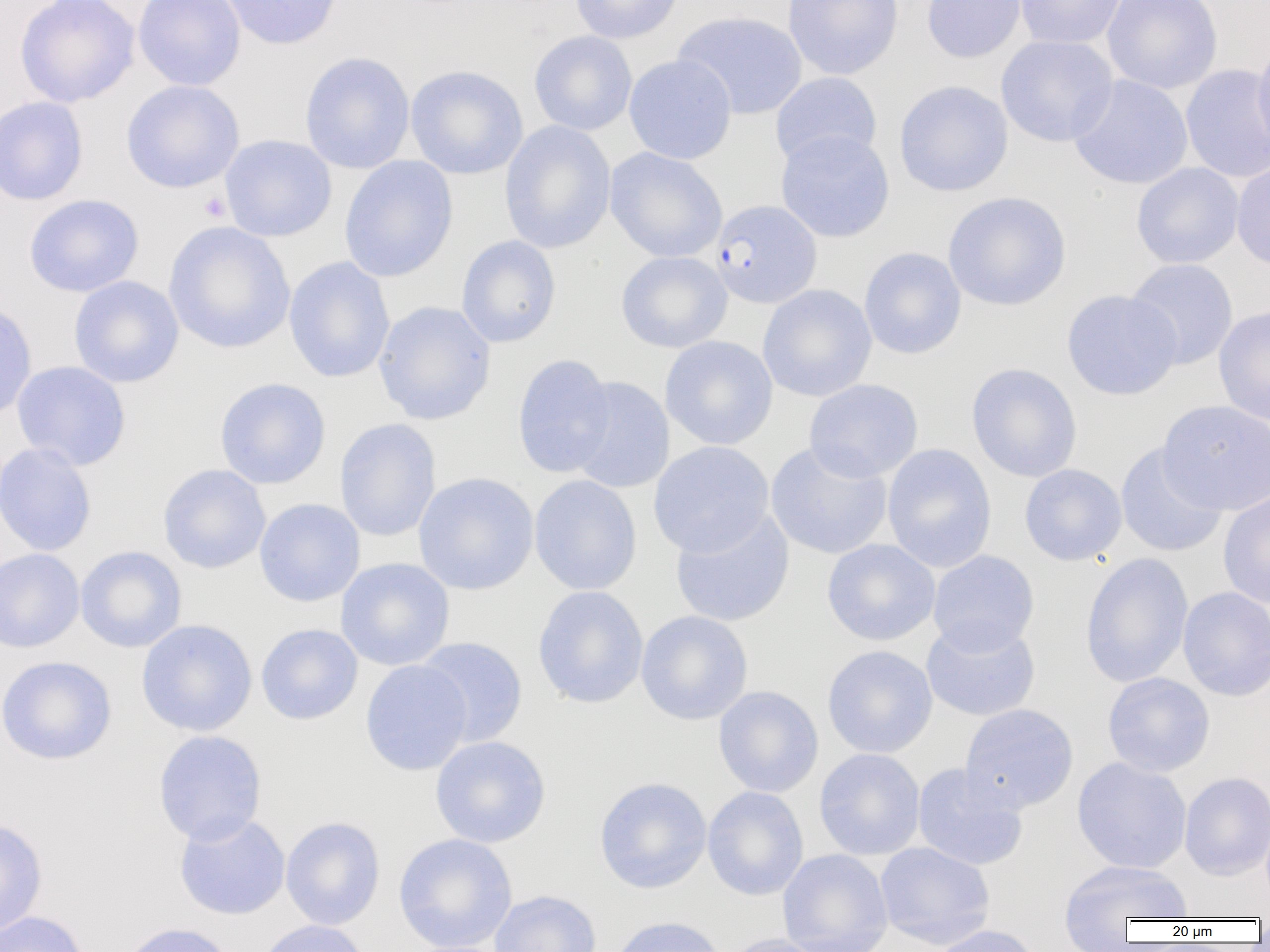 Approximate bounding boxes as [x1, y1, x2, y2] in pixels. Plasmodium falciparum-infected red blood cell locations: [710, 199, 822, 308]. Platelet locations: [199, 192, 232, 222]. Uninfected red blood cell locations: [15, 0, 140, 107], [133, 0, 245, 91], [220, 0, 344, 50], [569, 0, 683, 44], [783, 0, 904, 80], [921, 0, 1028, 63], [1014, 0, 1127, 49], [1102, 0, 1223, 94], [672, 10, 807, 120], [529, 31, 638, 136], [996, 34, 1118, 147], [1252, 36, 1270, 157], [299, 51, 415, 174], [624, 54, 737, 165], [1180, 63, 1270, 183], [406, 65, 528, 179], [770, 72, 882, 168], [1069, 75, 1193, 190], [121, 80, 244, 193], [894, 80, 1013, 197], [0, 95, 89, 206], [499, 120, 617, 254], [775, 129, 895, 243], [219, 134, 337, 242], [604, 147, 727, 262], [339, 156, 459, 283], [1232, 161, 1270, 272], [1131, 163, 1244, 268], [943, 191, 1072, 311], [23, 194, 144, 297], [164, 221, 295, 355], [456, 235, 561, 348], [859, 246, 967, 359], [616, 251, 733, 353], [283, 256, 395, 383], [1125, 258, 1238, 370], [68, 275, 184, 388], [757, 284, 877, 402], [1062, 289, 1182, 400], [0, 299, 37, 422], [373, 301, 497, 425], [1213, 306, 1270, 427], [659, 335, 778, 450], [512, 353, 616, 479], [11, 360, 131, 470], [966, 363, 1083, 482], [565, 376, 675, 493], [214, 377, 331, 489], [804, 379, 924, 482], [1158, 399, 1270, 515], [334, 417, 441, 542], [648, 441, 774, 557], [0, 442, 97, 557], [765, 442, 893, 560], [1115, 443, 1228, 558], [882, 444, 997, 572], [1019, 463, 1127, 566], [158, 464, 271, 574], [413, 472, 539, 595], [529, 475, 642, 596], [1218, 491, 1270, 608], [254, 498, 365, 607], [670, 509, 795, 627], [821, 539, 940, 646], [75, 546, 187, 653], [0, 548, 86, 653], [927, 549, 1040, 655], [1080, 552, 1194, 688], [335, 557, 455, 671], [532, 585, 648, 709], [1178, 586, 1270, 702], [635, 610, 753, 725], [921, 618, 1041, 721], [136, 619, 257, 736], [255, 623, 363, 726], [414, 637, 529, 746], [822, 645, 938, 758], [0, 655, 117, 765], [360, 659, 473, 776], [1102, 672, 1215, 777], [713, 686, 824, 798], [959, 703, 1079, 813], [152, 729, 268, 846], [430, 736, 551, 848], [813, 748, 926, 860], [1071, 757, 1192, 874], [912, 763, 1029, 871], [1179, 772, 1270, 881], [594, 777, 712, 894], [702, 786, 808, 900], [174, 812, 291, 920], [280, 816, 386, 930], [0, 817, 48, 938], [393, 833, 518, 952], [874, 841, 995, 949], [777, 849, 893, 952], [1059, 860, 1193, 933], [489, 889, 602, 952], [0, 910, 91, 952], [610, 915, 727, 952], [255, 919, 372, 952], [119, 921, 237, 952], [927, 924, 1044, 952], [718, 933, 832, 952]. Slide-level diagnosis: Plasmodium falciparum. Light microscopy. Image is 1270×952 pixels. One field of a larger specimen. 1000x magnification. Thin blood film.